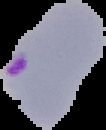

Summary:
  - Image size: 106×130 pixels
  - Result: Plasmodium parasites identified
  - Image type: cell region segmented out of the field of view; surrounding area masked to black
  - Preparation: thin blood smear